State the blood parasite species.
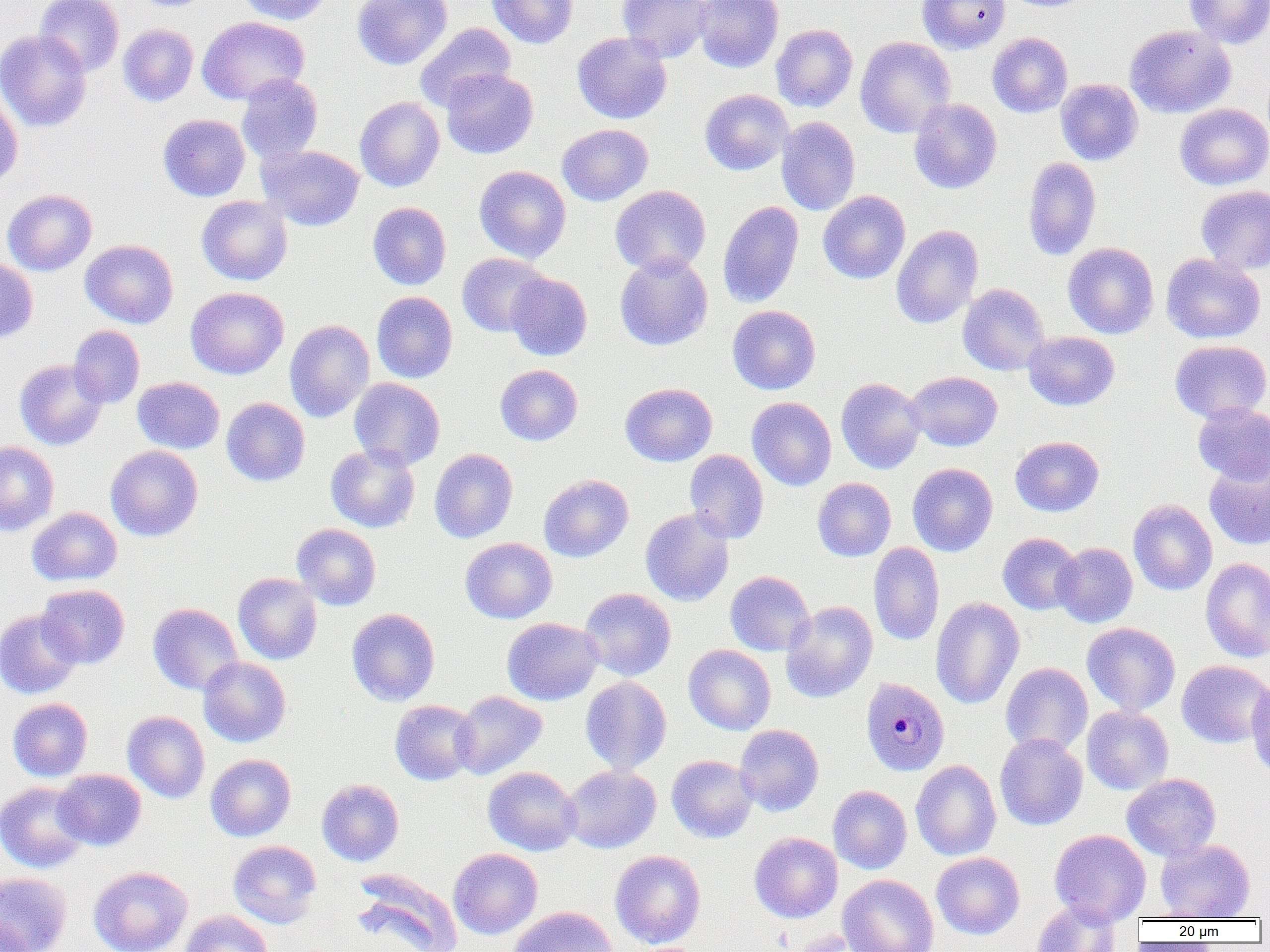
Plasmodium malariae.

magnification = 1000x
Plasmodium malariae-infected red blood cell locations = approximate bounding boxes as (x1, y1, x2, y2) in pixels: (860, 677, 949, 776)
image size = 1270×952 pixels
field of view = single
uninfected red blood cell locations = approximate bounding boxes as (x1, y1, x2, y2) in pixels: (34, 0, 125, 77), (234, 0, 332, 25), (352, 0, 452, 70), (486, 0, 578, 48), (617, 0, 714, 62), (693, 0, 783, 73), (917, 0, 1011, 54), (1184, 0, 1270, 49), (197, 16, 309, 105), (414, 22, 516, 111), (118, 24, 198, 106), (771, 24, 858, 112), (1124, 25, 1236, 118), (0, 30, 92, 132), (572, 32, 672, 124), (987, 32, 1072, 118), (855, 36, 956, 138), (440, 69, 538, 158), (235, 74, 323, 164), (1055, 78, 1143, 165), (700, 89, 793, 175), (0, 91, 23, 190), (355, 96, 444, 192), (909, 98, 1002, 194), (1174, 103, 1270, 190), (158, 114, 250, 201), (776, 116, 860, 215), (557, 123, 653, 205), (258, 144, 364, 231), (1023, 156, 1101, 260), (474, 165, 571, 263), (1195, 184, 1270, 274), (610, 185, 711, 276), (2, 188, 97, 276), (818, 190, 911, 283), (197, 195, 292, 285), (368, 201, 451, 290), (717, 201, 804, 309), (891, 225, 983, 329), (80, 240, 178, 328), (1063, 242, 1159, 339), (615, 252, 713, 350), (457, 253, 552, 337), (1161, 253, 1265, 343), (0, 256, 38, 343), (505, 272, 592, 361), (957, 283, 1050, 375), (186, 287, 288, 379), (371, 291, 457, 383), (727, 305, 820, 394), (284, 319, 374, 422), (68, 325, 145, 408), (1023, 331, 1119, 410), (1170, 340, 1270, 423), (14, 358, 107, 451), (495, 365, 582, 445), (907, 371, 1002, 451), (132, 377, 225, 454), (349, 377, 445, 470), (836, 378, 926, 474), (620, 383, 717, 466), (221, 397, 310, 486), (747, 397, 837, 490), (1193, 402, 1270, 484), (1010, 436, 1104, 516), (0, 441, 59, 536), (325, 444, 420, 532), (105, 445, 203, 542), (429, 448, 518, 543), (684, 449, 769, 543), (1204, 459, 1270, 550), (907, 463, 998, 556), (538, 474, 633, 562), (813, 477, 896, 561), (1128, 499, 1217, 596), (27, 507, 122, 586), (640, 508, 734, 607), (291, 523, 381, 610), (997, 532, 1082, 615), (460, 537, 557, 624), (869, 541, 945, 646), (1052, 542, 1138, 628), (1201, 557, 1270, 662), (725, 570, 816, 656), (233, 573, 322, 664), (37, 584, 130, 668), (579, 588, 676, 681), (930, 597, 1024, 709), (780, 601, 878, 703), (148, 602, 243, 695), (346, 608, 440, 706), (0, 609, 83, 699), (502, 617, 603, 705), (1082, 622, 1180, 715), (684, 644, 776, 735), (198, 656, 291, 747), (1176, 660, 1270, 748), (1000, 662, 1093, 755), (1246, 674, 1270, 781), (580, 676, 671, 773), (450, 690, 547, 779), (8, 698, 92, 782), (390, 699, 480, 785), (1081, 706, 1173, 795), (122, 711, 210, 803), (734, 724, 824, 816), (994, 733, 1088, 830), (205, 754, 295, 841), (666, 754, 758, 843), (911, 760, 1001, 860), (562, 764, 660, 853), (483, 766, 581, 855), (53, 769, 146, 851), (1122, 773, 1221, 861), (317, 779, 404, 866), (0, 781, 90, 873), (828, 785, 912, 874), (1049, 829, 1151, 925), (749, 832, 843, 922), (1155, 838, 1255, 920), (228, 840, 322, 928), (448, 848, 543, 939), (610, 850, 706, 948), (931, 852, 1024, 939), (88, 865, 193, 952), (351, 869, 463, 952), (0, 871, 72, 952), (838, 874, 939, 952), (1032, 901, 1121, 952), (507, 905, 617, 952), (180, 910, 273, 952), (1, 916, 35, 952), (780, 931, 876, 952)
modality = optical microscopy
preparation = thin blood film